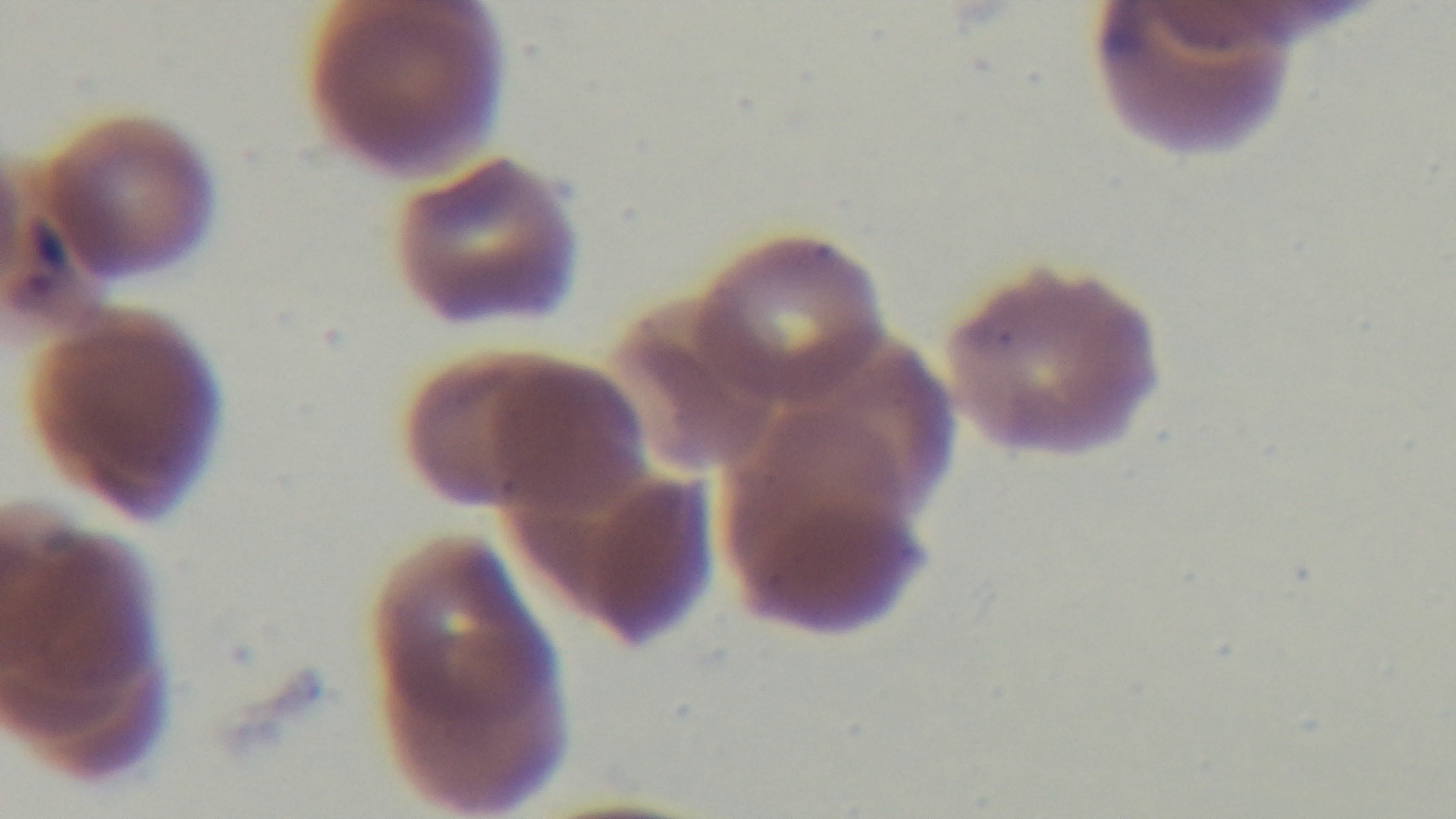
preparation = thin
stain = Giemsa
malaria status = positive
modality = light microscopy
objective = 100x oil immersion
capture = mounted 4K digital camera
field of view = one from the slide